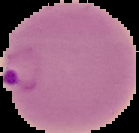

Summary:
  - Preparation: thin blood film
  - Image type: cell region segmented out of the field of view; surrounding area masked to black
  - Image size: 139×133 pixels
  - Malaria status: parasitized